Point out each Plasmodium parasite.
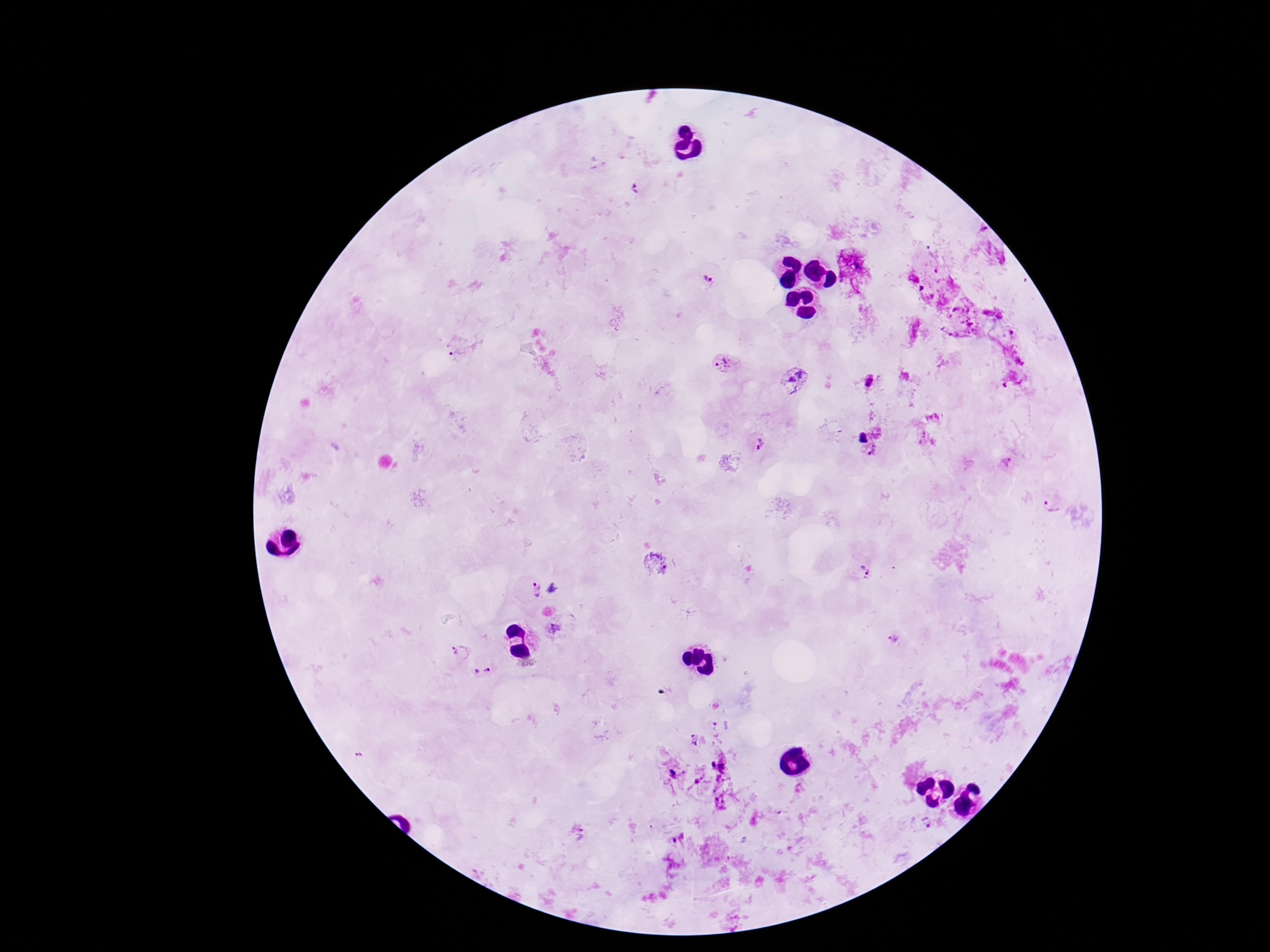

Approximate centers as {x, y} in pixels.
Plasmodium parasites: {636, 191}, {707, 278}, {458, 347}, {720, 361}, {796, 378}, {869, 380}, {760, 445}, {1052, 504}, {863, 573}, {555, 588}, {536, 589}, {556, 628}, {894, 638}, {458, 651}, {482, 671}, {694, 739}, {928, 823}, {582, 834}.

Summary:
  - Capture: smartphone camera through the microscope eyepiece
  - Magnification: 100x
  - Preparation: thick blood film
  - Field of view: single
  - Stain: Giemsa
  - Patient malaria status: positive
  - Image size: 1270×952 pixels